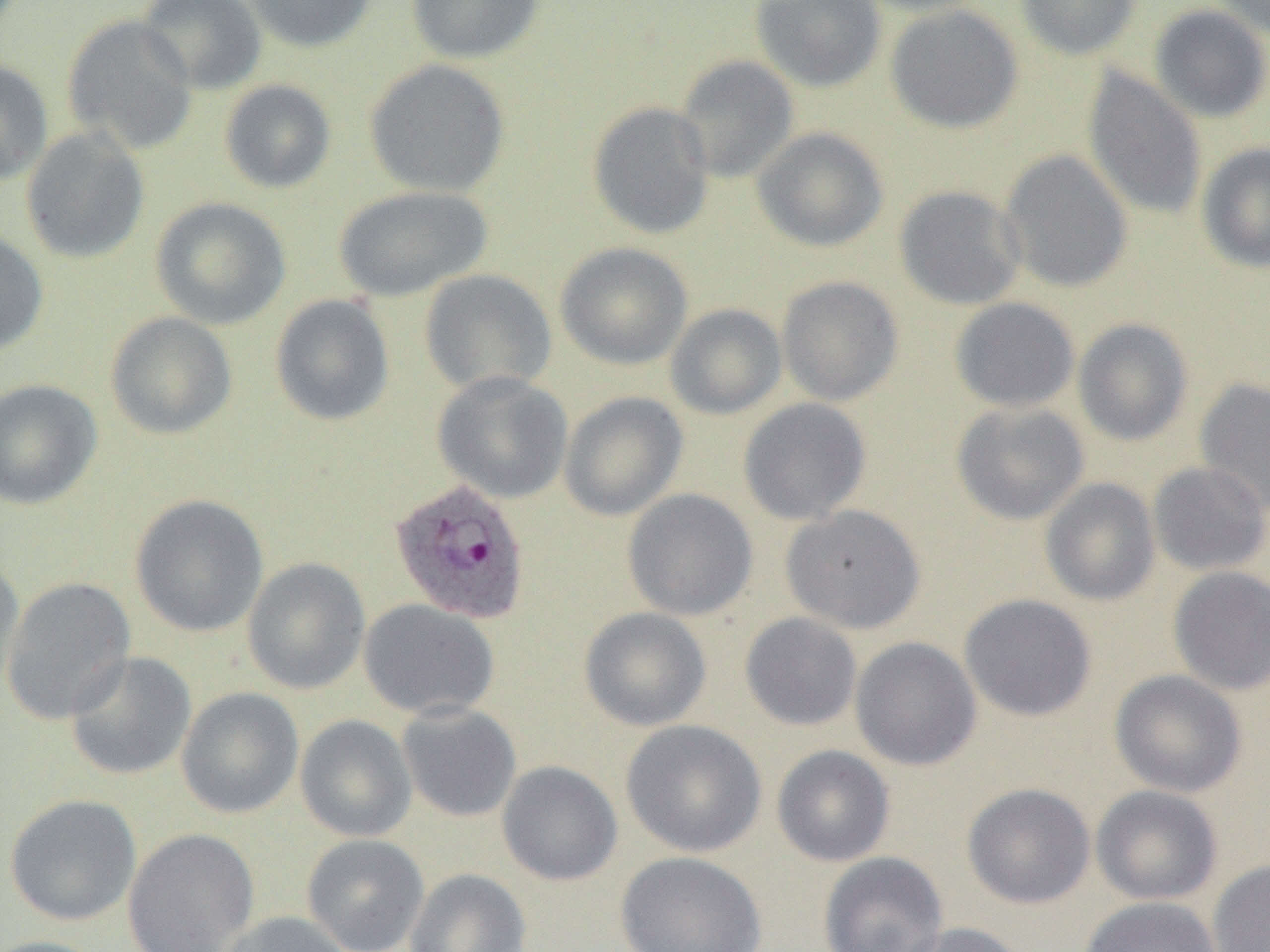

{
  "slide_level_diagnosis": "Plasmodium ovale",
  "preparation": "thin blood smear",
  "modality": "light microscopy",
  "image_size": "1270×952 pixels",
  "field_of_view": "one of a larger specimen",
  "plasmodium_ovale_infected_red_blood_cell_locations": "approximate bounding boxes as named x1/y1/x2/y2 corners in pixels: (x1=388, y1=477, x2=531, y2=624)",
  "uninfected_red_blood_cell_locations": "approximate bounding boxes as named x1/y1/x2/y2 corners in pixels: (x1=136, y1=0, x2=268, y2=95), (x1=241, y1=0, x2=378, y2=52), (x1=405, y1=0, x2=546, y2=64), (x1=750, y1=0, x2=887, y2=92), (x1=853, y1=0, x2=994, y2=16), (x1=1015, y1=0, x2=1143, y2=60), (x1=1209, y1=0, x2=1270, y2=40), (x1=885, y1=4, x2=1023, y2=134), (x1=1149, y1=4, x2=1270, y2=123), (x1=62, y1=14, x2=199, y2=156), (x1=673, y1=54, x2=799, y2=183), (x1=363, y1=58, x2=511, y2=198), (x1=0, y1=59, x2=54, y2=187), (x1=1082, y1=68, x2=1207, y2=220), (x1=218, y1=80, x2=337, y2=194), (x1=587, y1=101, x2=715, y2=240), (x1=20, y1=127, x2=150, y2=265), (x1=751, y1=127, x2=890, y2=253), (x1=1197, y1=142, x2=1270, y2=274), (x1=998, y1=149, x2=1133, y2=293), (x1=333, y1=185, x2=494, y2=302), (x1=894, y1=185, x2=1027, y2=310), (x1=149, y1=197, x2=292, y2=330), (x1=0, y1=229, x2=49, y2=357), (x1=555, y1=241, x2=693, y2=370), (x1=419, y1=269, x2=558, y2=396), (x1=776, y1=276, x2=904, y2=406), (x1=269, y1=294, x2=395, y2=427), (x1=949, y1=297, x2=1080, y2=412), (x1=665, y1=303, x2=787, y2=419), (x1=104, y1=311, x2=238, y2=440), (x1=1073, y1=318, x2=1193, y2=446), (x1=432, y1=371, x2=573, y2=503), (x1=1194, y1=377, x2=1270, y2=516), (x1=0, y1=378, x2=102, y2=510), (x1=559, y1=391, x2=688, y2=521), (x1=738, y1=397, x2=872, y2=525), (x1=951, y1=400, x2=1090, y2=525), (x1=1147, y1=461, x2=1270, y2=577), (x1=1040, y1=477, x2=1161, y2=606), (x1=621, y1=488, x2=758, y2=621), (x1=130, y1=493, x2=269, y2=637), (x1=780, y1=504, x2=927, y2=633), (x1=0, y1=552, x2=25, y2=697), (x1=242, y1=557, x2=371, y2=694), (x1=1168, y1=566, x2=1270, y2=695), (x1=1, y1=576, x2=137, y2=725), (x1=959, y1=593, x2=1097, y2=721), (x1=358, y1=598, x2=500, y2=721), (x1=579, y1=607, x2=712, y2=731), (x1=739, y1=612, x2=863, y2=731), (x1=850, y1=636, x2=982, y2=770), (x1=64, y1=651, x2=197, y2=781), (x1=1110, y1=669, x2=1247, y2=798), (x1=176, y1=687, x2=304, y2=819), (x1=397, y1=702, x2=522, y2=823), (x1=295, y1=714, x2=417, y2=842), (x1=620, y1=719, x2=768, y2=858), (x1=771, y1=744, x2=895, y2=867), (x1=496, y1=760, x2=623, y2=886), (x1=961, y1=782, x2=1095, y2=909), (x1=1090, y1=785, x2=1223, y2=906), (x1=4, y1=794, x2=142, y2=927), (x1=122, y1=827, x2=260, y2=951), (x1=301, y1=833, x2=429, y2=952), (x1=614, y1=850, x2=767, y2=952), (x1=818, y1=851, x2=949, y2=952), (x1=1208, y1=860, x2=1270, y2=952), (x1=404, y1=868, x2=533, y2=952), (x1=1079, y1=896, x2=1223, y2=952), (x1=216, y1=911, x2=353, y2=952), (x1=894, y1=921, x2=1032, y2=952), (x1=0, y1=935, x2=107, y2=952)",
  "magnification": "1000x"
}